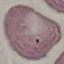

malaria status = uninfected
preparation = thin smear
capture = smartphone camera at the microscope eyepiece
stain = Giemsa
image type = cell patch, automatically extracted from a larger field of view and resized to 64 × 64 pixels